Comment on the morphology of the erythrocytes.
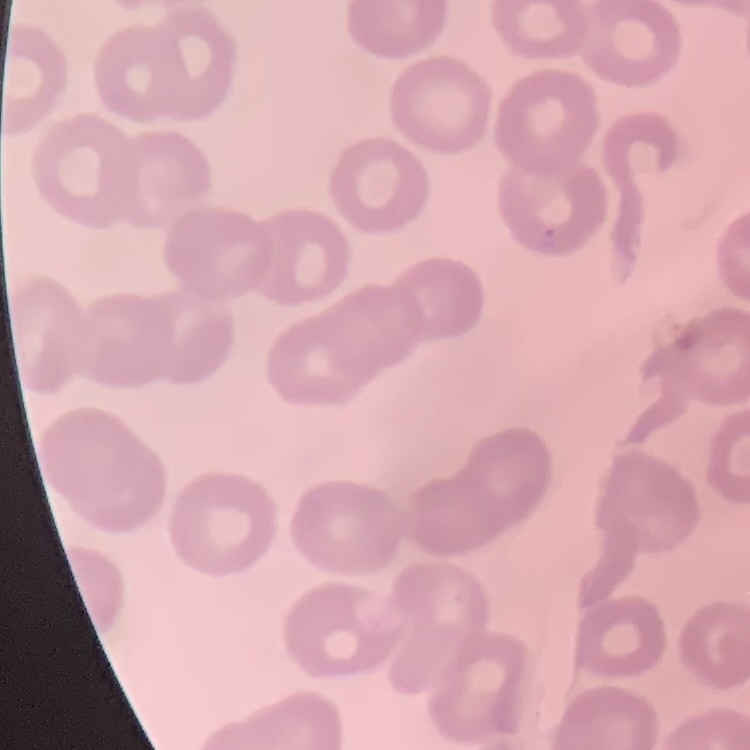
They show no rouleaux formation.

preparation = thin peripheral smear
stain = Field's or Giemsa
image type = one tile cut from a larger photomicrograph